Identify the preparation type.
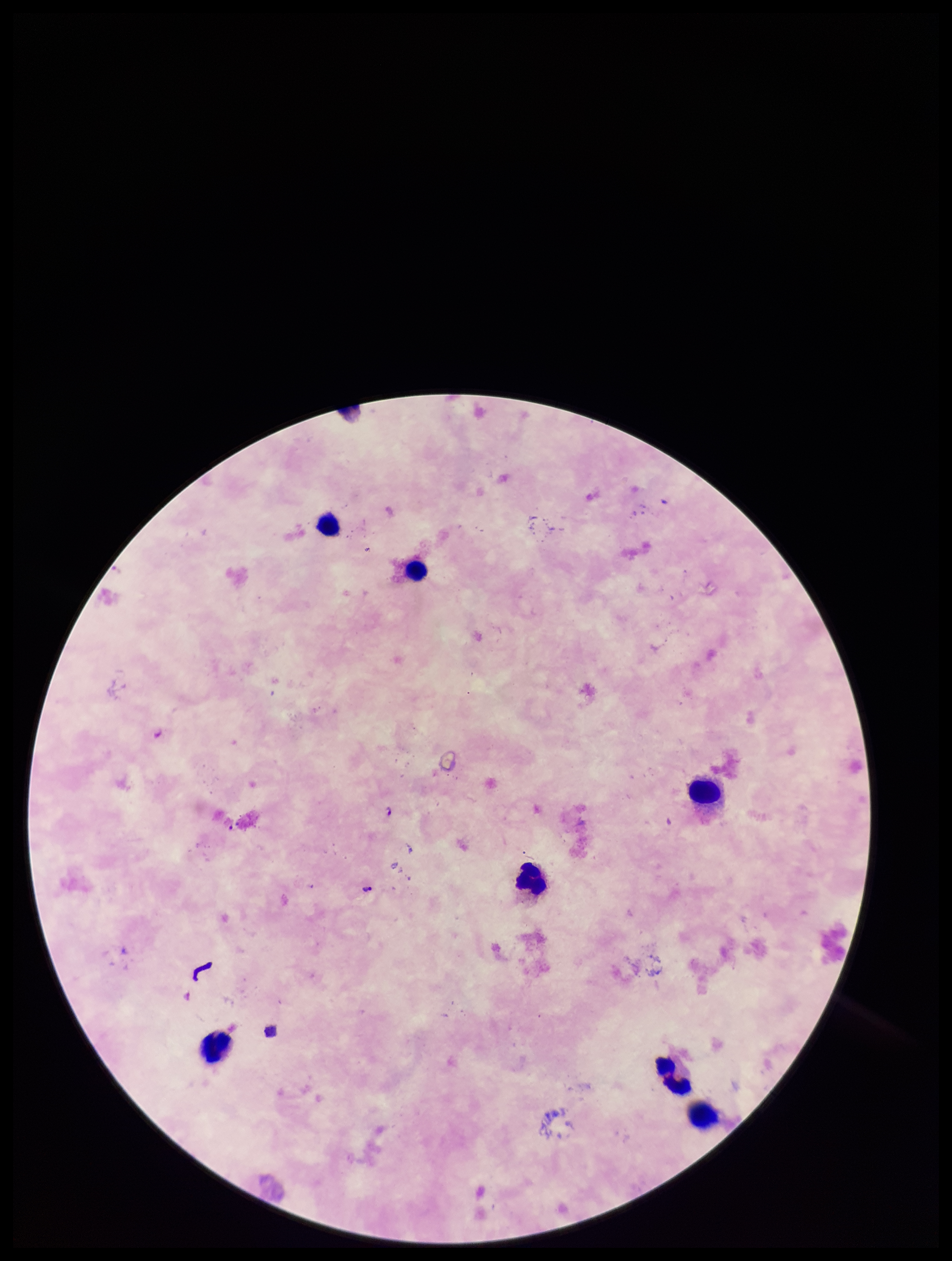
A thick smear.

field of view = single
image size = 952×1261 pixels
leukocyte count = 7
capture = smartphone photograph through the microscope eyepiece
parasite count = 2
patient malaria status = positive
stain = Giemsa
species reported for this patient = Plasmodium falciparum
Plasmodium parasites = seen